Describe the morphology of the red blood cells.
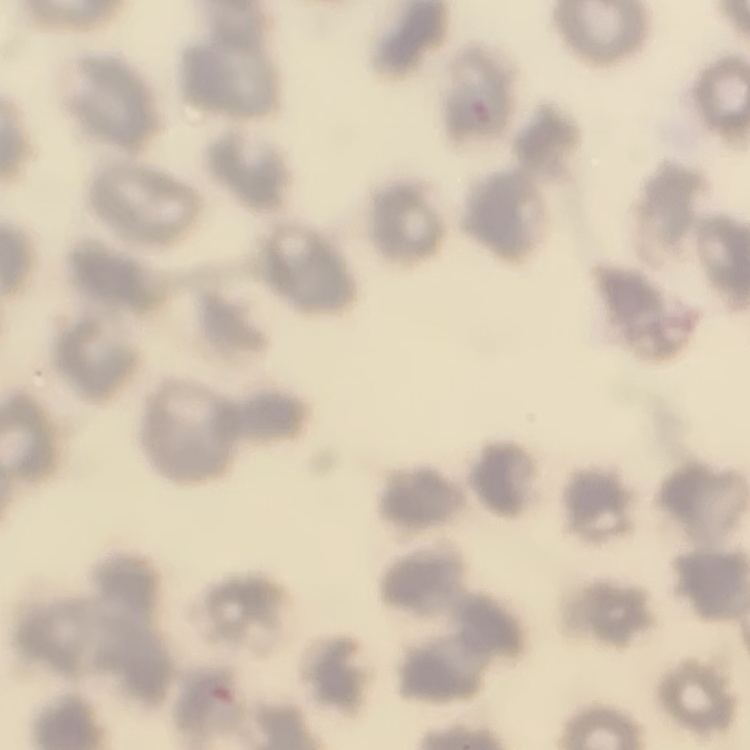

No rouleaux formation.

Thin blood film. Square crop of a larger photomicrograph. Stained with either Field's or Giemsa.